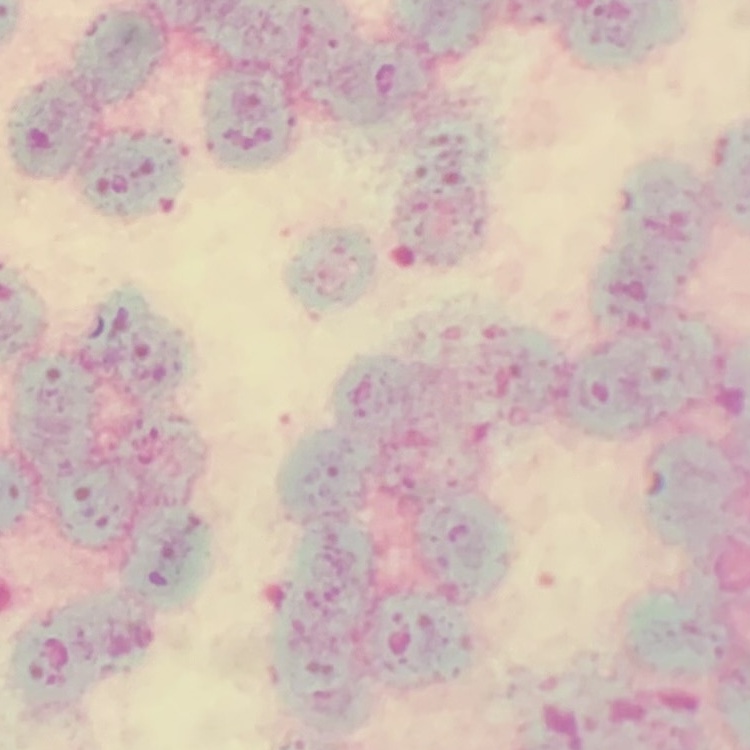 The red blood cells exhibit rouleaux formation. Thin blood film. Field's or Giemsa stain. One tile cut from a larger photomicrograph.